Describe the morphology of the red blood cells.
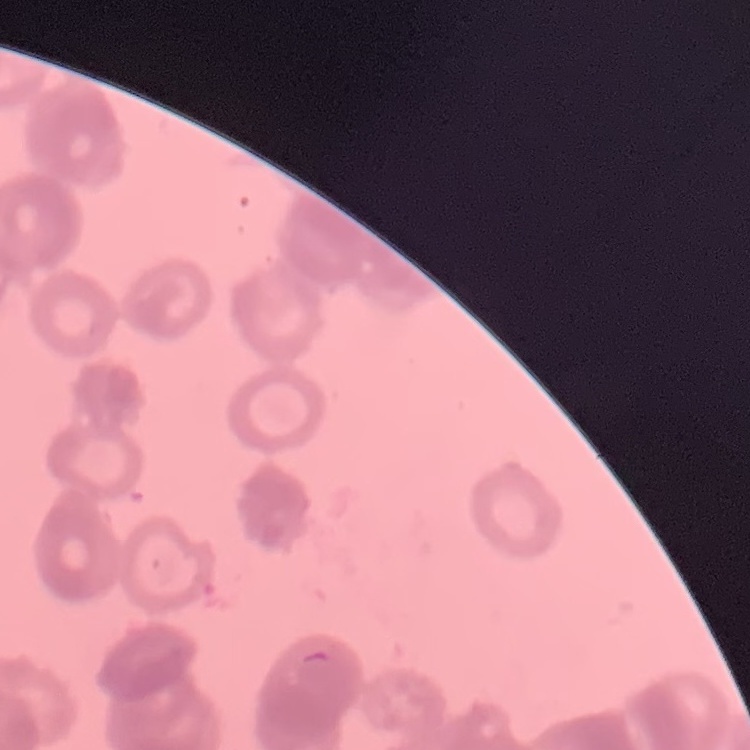

They show rouleaux formation.

Square crop of a larger photomicrograph. Thin blood film. Field's or Giemsa stain.